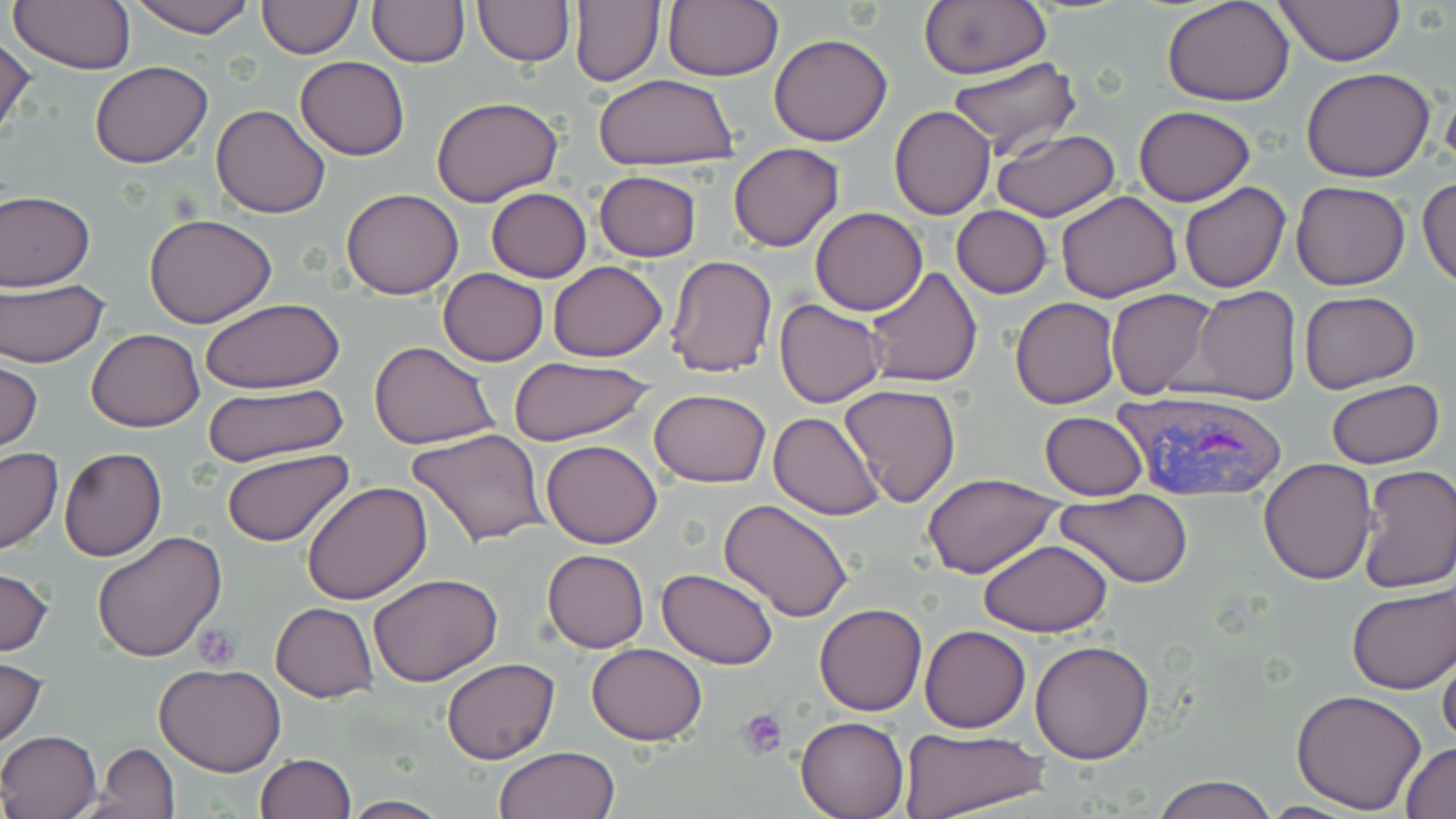
Summary:
  - Coordinate format: approximate bounding boxes as (x1,y1)-(x2,y2) corner pairs in pixels
  - Uninfected red blood cell locations: (127,0)-(256,38), (256,0)-(362,57), (567,0)-(667,87), (661,0)-(784,84), (918,0)-(1050,80), (1162,0)-(1295,105), (1274,0)-(1405,67), (8,1)-(134,74), (367,1)-(467,68), (472,1)-(574,66), (769,32)-(893,146), (0,36)-(36,142), (948,56)-(1080,157), (295,57)-(410,160), (90,61)-(214,167), (1302,66)-(1436,182), (591,74)-(739,170), (431,95)-(562,205), (210,103)-(332,218), (889,105)-(996,219), (1133,105)-(1255,206), (991,128)-(1120,221), (729,142)-(845,252), (593,171)-(702,262), (1417,178)-(1456,290), (1291,181)-(1411,291), (1178,182)-(1290,293), (341,187)-(464,300), (485,187)-(592,282), (0,189)-(96,291), (1056,191)-(1182,303), (951,205)-(1053,298), (809,206)-(928,315), (143,211)-(279,328), (665,254)-(778,377), (548,260)-(666,362), (863,267)-(982,388), (438,268)-(548,367), (0,280)-(108,367), (1189,286)-(1302,406), (1105,288)-(1219,401), (1299,289)-(1421,394), (1009,296)-(1121,409), (202,299)-(346,394), (774,299)-(886,408), (86,328)-(206,431), (369,340)-(499,450), (508,356)-(659,449), (0,359)-(42,454), (1327,378)-(1444,469), (839,383)-(962,507), (203,384)-(349,468), (649,389)-(772,488), (768,411)-(883,520), (1039,411)-(1149,500), (408,427)-(551,547), (540,440)-(663,548), (0,447)-(64,556), (58,448)-(166,561), (220,448)-(355,548), (1258,460)-(1377,586), (1357,464)-(1456,593), (922,475)-(1064,579), (301,481)-(434,605), (1056,494)-(1193,586), (719,499)-(854,622), (92,531)-(227,663), (978,540)-(1113,635), (542,549)-(650,653), (0,565)-(56,658), (656,568)-(779,669), (367,573)-(504,686), (1345,584)-(1454,695), (271,603)-(377,702), (813,604)-(926,716), (919,625)-(1032,733), (1030,639)-(1154,763), (587,642)-(707,745), (1437,643)-(1456,751), (1,655)-(49,749), (441,657)-(560,765), (154,662)-(285,777), (1292,689)-(1426,813), (796,716)-(908,818), (897,727)-(1052,819), (0,730)-(103,818), (1402,742)-(1456,818), (95,743)-(180,816), (494,745)-(620,819), (255,752)-(355,818), (1152,775)-(1278,819), (340,794)-(449,817)
  - Plasmodium vivax-infected red blood cell locations: (1112,384)-(1291,503)
  - Platelet locations: (192,622)-(243,670), (738,710)-(787,758)
  - Slide-level diagnosis: Plasmodium vivax
  - Modality: light microscopy
  - Preparation: thin blood smear
  - Stain: May-Grünwald-Giemsa
  - Field of view: one of a larger specimen
  - Magnification: 1000x
  - Image size: 1456×819 pixels